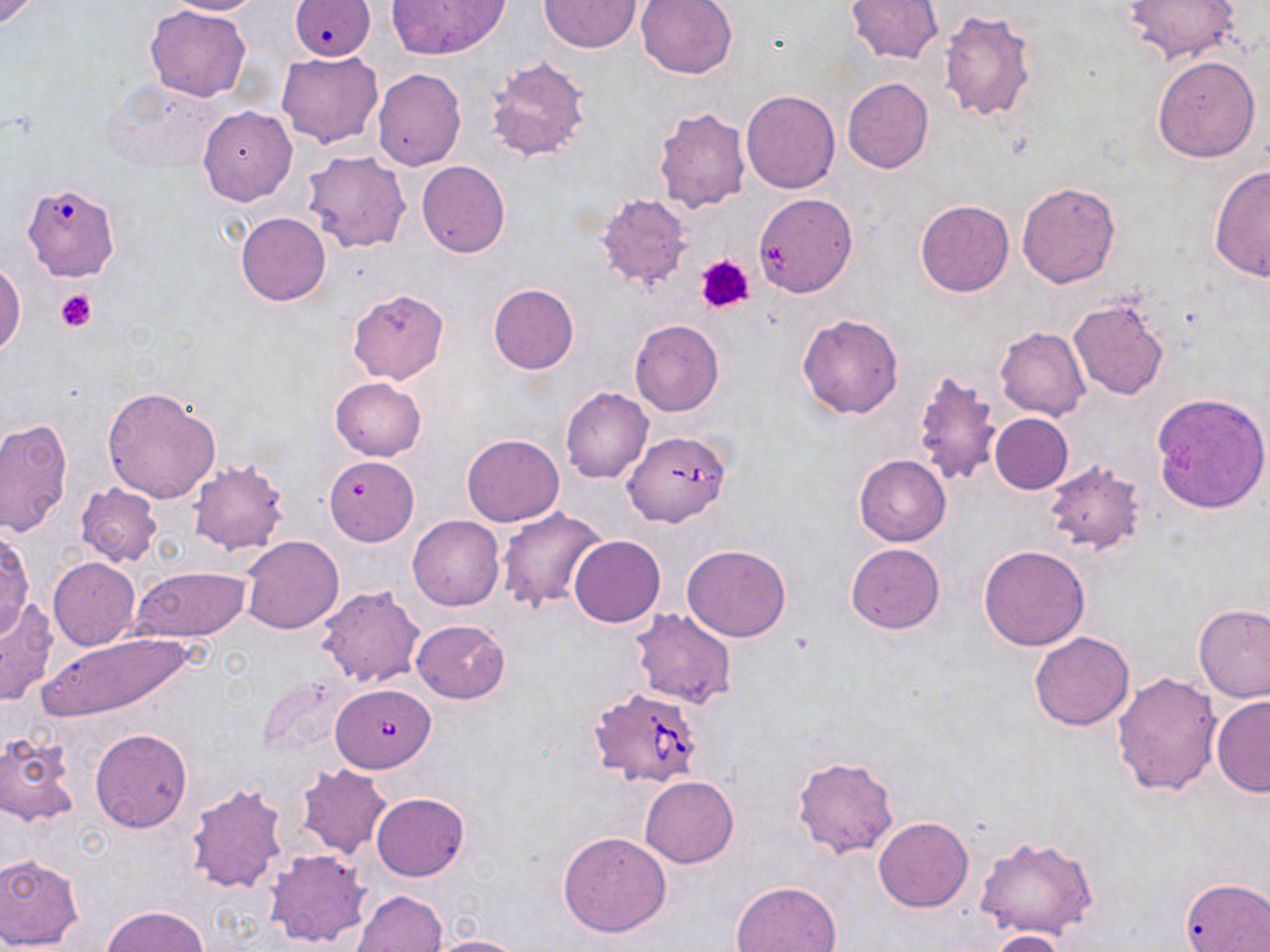
Approximate bounding boxes as (x1, y1, x2, y2) in pixels. Babesia divergens-infected red blood cell locations: (622, 430, 730, 527), (324, 682, 445, 779), (589, 686, 708, 792). Uninfected red blood cell locations: (0, 0, 41, 30), (163, 0, 264, 15), (386, 0, 510, 59), (634, 0, 740, 79), (847, 0, 943, 65), (1121, 0, 1240, 65), (537, 1, 643, 52), (146, 5, 252, 101), (938, 10, 1038, 122), (276, 51, 383, 148), (485, 53, 592, 163), (1153, 55, 1261, 162), (372, 68, 466, 170), (843, 77, 933, 172), (103, 79, 231, 175), (741, 89, 840, 193), (666, 101, 832, 204), (196, 105, 296, 205), (653, 105, 752, 213), (302, 150, 411, 253), (416, 160, 510, 259), (1210, 164, 1270, 282), (1016, 181, 1120, 288), (27, 187, 121, 284), (595, 193, 693, 292), (754, 193, 856, 297), (915, 200, 1013, 297), (235, 212, 331, 306), (1, 259, 25, 356), (488, 283, 579, 374), (348, 288, 449, 384), (1068, 298, 1170, 401), (797, 313, 904, 418), (629, 320, 724, 416), (994, 327, 1090, 421), (911, 369, 1005, 484), (329, 376, 427, 461), (561, 386, 653, 483), (102, 387, 219, 503), (1151, 392, 1269, 513), (990, 413, 1073, 494), (0, 416, 72, 537), (462, 433, 564, 527), (854, 455, 950, 546), (186, 459, 290, 555), (1042, 460, 1147, 554), (322, 461, 419, 547), (75, 483, 163, 568), (495, 507, 606, 615), (408, 515, 504, 611), (0, 528, 35, 639), (569, 535, 664, 628), (240, 536, 344, 634), (847, 542, 944, 632), (681, 543, 792, 642), (978, 545, 1091, 651), (48, 557, 140, 651), (130, 567, 251, 642), (315, 585, 426, 687), (0, 598, 60, 703), (1193, 603, 1270, 703), (630, 608, 737, 709), (411, 619, 510, 703), (31, 631, 197, 722), (1029, 631, 1134, 731), (1061, 653, 1200, 770), (1113, 672, 1223, 797), (1210, 696, 1270, 797), (90, 728, 193, 833), (0, 731, 79, 827), (792, 755, 898, 859), (294, 765, 393, 860), (640, 775, 738, 867), (184, 781, 289, 895), (370, 793, 470, 881), (874, 817, 973, 912), (557, 831, 670, 937), (973, 836, 1101, 938), (265, 848, 372, 951), (0, 853, 85, 949), (1179, 878, 1270, 952), (731, 880, 842, 952), (352, 890, 447, 952), (102, 905, 207, 951), (987, 930, 1066, 952), (418, 935, 525, 952). Platelet locations: (697, 254, 753, 314), (55, 289, 96, 332). Slide-level diagnosis: Babesia divergens. May-Grünwald-Giemsa-stained preparation. Captured at 1000x magnification. Thin blood smear. Image is 1270×952 pixels. Single field of view. Optical microscopy.